Classify this cell by malaria status.
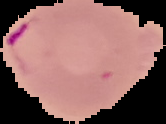
Parasitized.

Cell region segmented out of the field of view; the surrounding area is masked to black. From a thin blood smear. Image is 166×124 pixels.